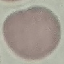

Result: no malaria parasites detected. Cell patch, automatically extracted from a larger field of view and resized to 64 × 64 pixels. Giemsa-stained preparation. Photographed with a smartphone camera at the microscope eyepiece. Thin smear of blood.